State which parasite is depicted.
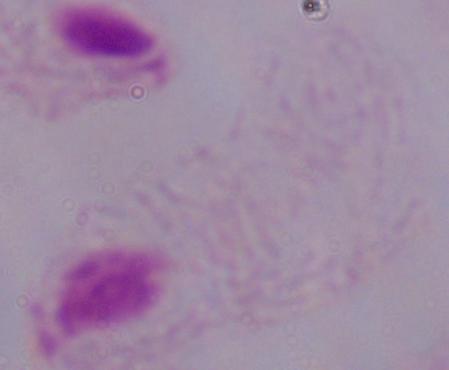

This is a trichomonad.

Micrograph. Captured at 1000x magnification.